Give the position of every malaria parasite.
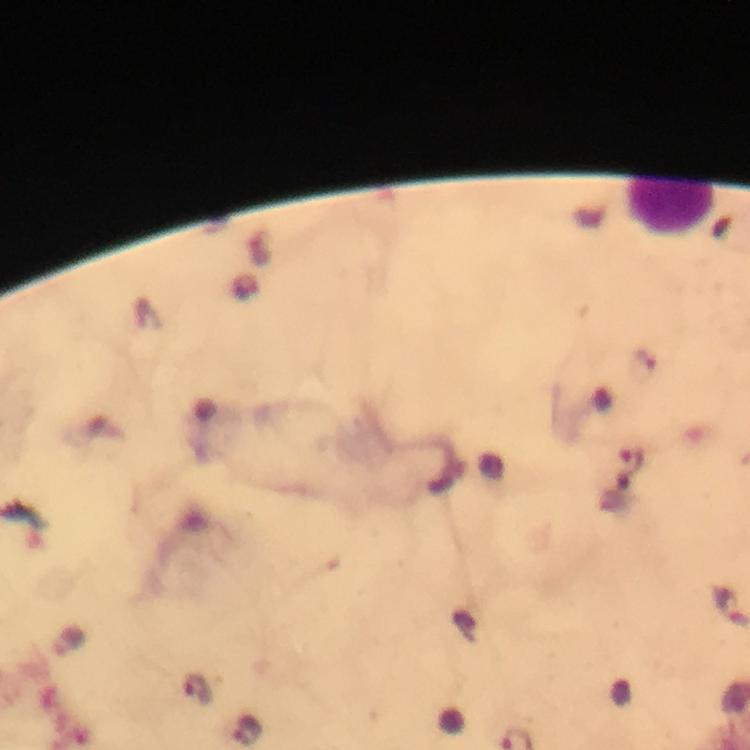

Approximate object centers, in pixels from the top-left corner.
Malaria parasites: (x=631, y=461), (x=728, y=606), (x=197, y=688), (x=248, y=730).

Summary:
  - Leukocyte locations: (x=668, y=206)
  - Capture: smartphone mounted on the microscope
  - Image size: 750×750 pixels
  - Preparation: thick smear
  - Context: from a diagnostic examination for malaria
  - Stain: Giemsa
  - Immersion oil: used
  - Cropped from: one field of view
  - Magnification: 100x